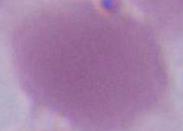

Photomicrograph. An erythrocyte is seen. 1000x magnification.